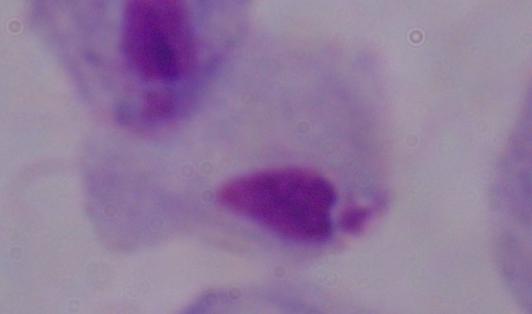

Summary:
  - Identification: trichomonad
  - Modality: micrograph
  - Magnification: 1000x